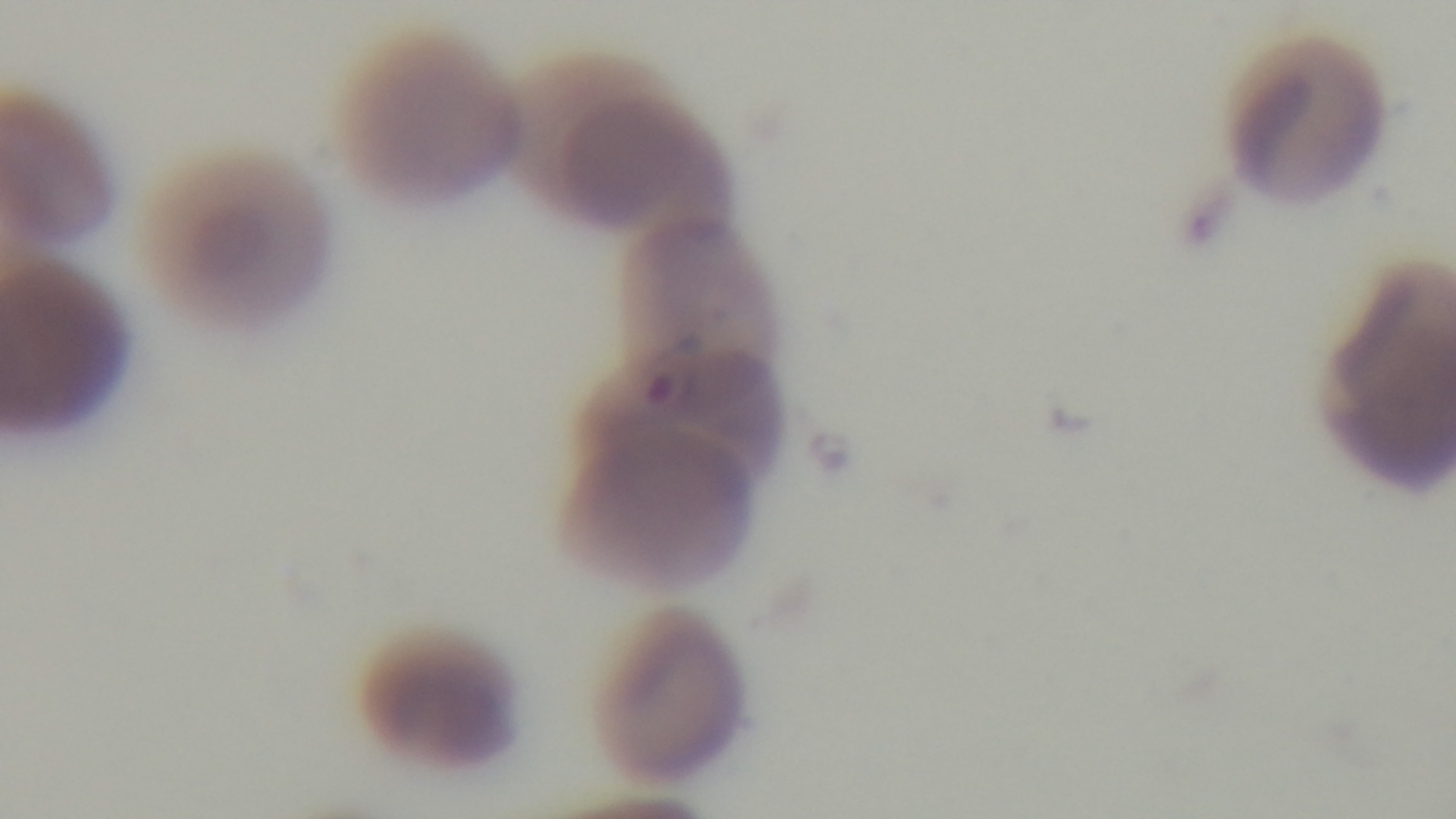
Summary:
  - Modality: light microscopy
  - Malaria status: infected
  - Objective: 100x oil immersion
  - Field of view: single
  - Stain: Giemsa
  - Preparation: thin
  - Capture: mounted 4K digital camera